Point out every malaria parasite.
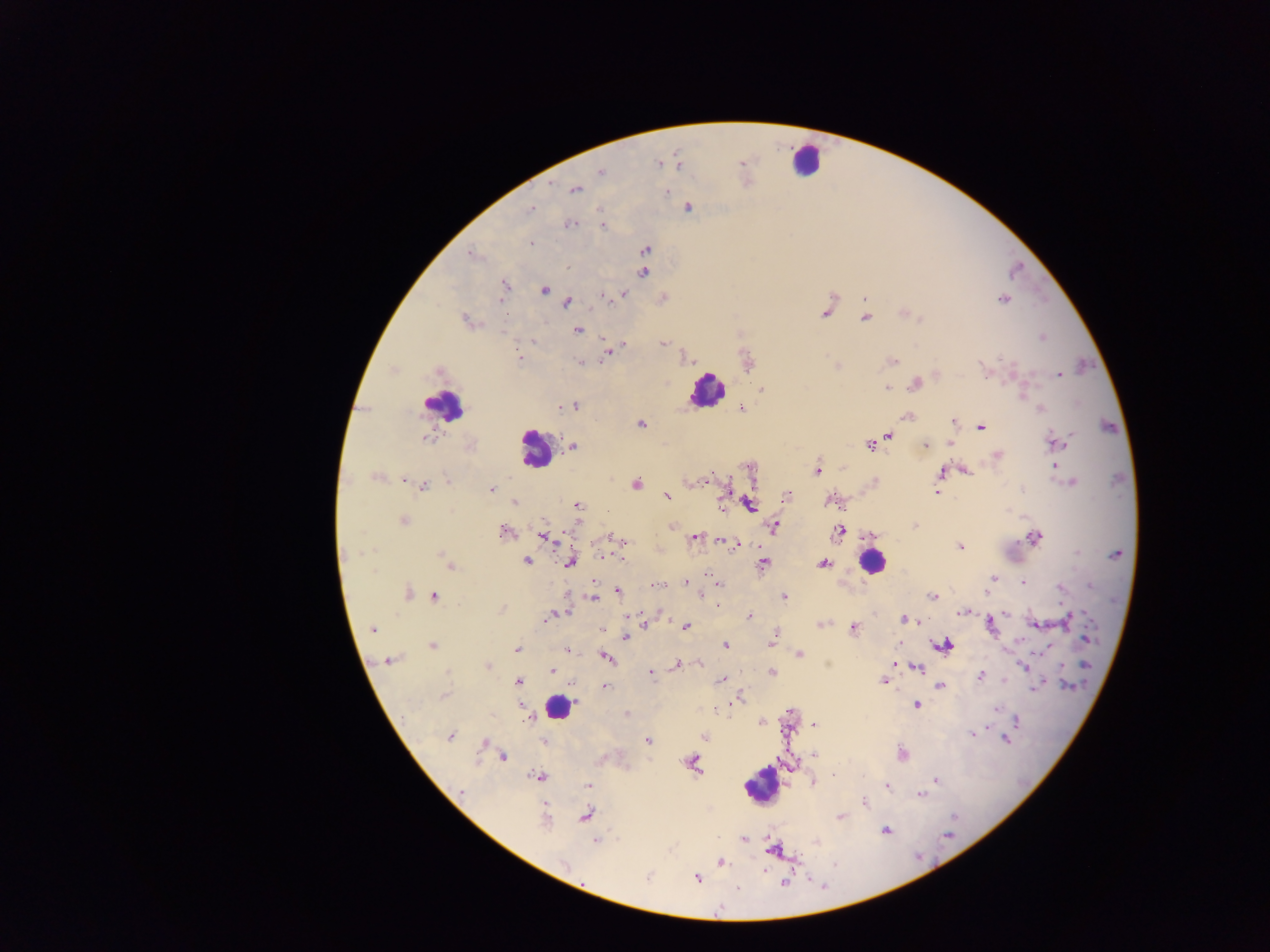

Approximate centers as x y in pixels.
Malaria parasites: 659 163; 742 163; 600 172; 575 189; 666 192; 532 208; 687 208; 599 211; 570 223; 603 225; 531 243; 646 250; 472 254; 567 267; 643 273; 504 286; 545 290; 622 293; 602 296; 865 298; 1003 299; 567 302; 824 313; 865 318; 465 320; 577 330; 1042 337; 532 341; 662 343; 623 344; 608 353; 518 359; 689 360; 893 361; 581 363; 837 365; 982 366; 1059 375; 916 384; 887 388; 762 389; 1023 395; 574 406; 560 407; 741 409; 1041 409; 907 416; 953 421; 640 423; 982 427; 888 435; 426 438; 1064 440; 1056 442; 951 444; 869 445; 925 445; 572 446; 998 455; 1053 466; 818 469; 966 470; 941 472; 375 477; 404 479; 708 479; 447 480; 1070 483; 636 484; 423 487; 491 490; 937 492; 788 495; 667 496; 515 502; 722 504; 750 505; 578 506; 403 521; 914 525; 672 526; 774 526; 503 532; 839 532; 545 537; 1034 537; 615 538; 695 538; 723 540; 960 547; 1077 553; 1115 554; 440 555; 602 556; 621 557; 527 561; 571 561; 763 564; 824 564; 449 565; 374 572; 992 578; 1023 582; 685 583; 719 585; 656 586; 1090 586; 1060 588; 618 591; 407 592; 434 596; 593 596; 932 596; 701 597; 784 597; 717 605; 501 609; 566 611; 963 612; 1005 613; 556 614; 750 616; 547 617; 1068 619; 905 620; 824 624; 1036 624; 992 625; 686 626; 373 629; 853 629; 601 630; 774 636; 625 637; 1085 638; 432 645; 725 645; 944 645; 517 650; 567 650; 799 655; 606 657; 389 660; 894 663; 699 664; 1086 664; 678 665; 487 666; 1024 666; 917 667; 552 671; 650 673; 772 673; 981 675; 723 680; 518 681; 883 681; 1067 685; 1035 686; 604 687; 940 687; 444 696; 736 701; 916 705; 996 708; 791 712; 626 714; 1017 721; 763 723; 814 724; 972 733; 449 736; 704 737; 1005 739; 648 740; 544 742; 484 743; 902 754; 815 755; 503 757; 693 763; 834 776; 538 777; 935 780; 814 782; 588 785; 888 786; 461 791; 920 795; 865 803; 585 815; 840 816; 544 821; 886 831; 947 835; 743 840; 597 841; 771 849; 721 862; 563 864; 648 878; 696 878; 784 883.

capture = mobile-phone photograph through a microscope
image size = 1270×952 pixels
leukocyte locations = approximate centers as x y in pixels: 806 159; 707 389; 443 405; 534 449; 872 562; 558 708; 763 785
country = Ghana
preparation = thick blood smear
field of view = single